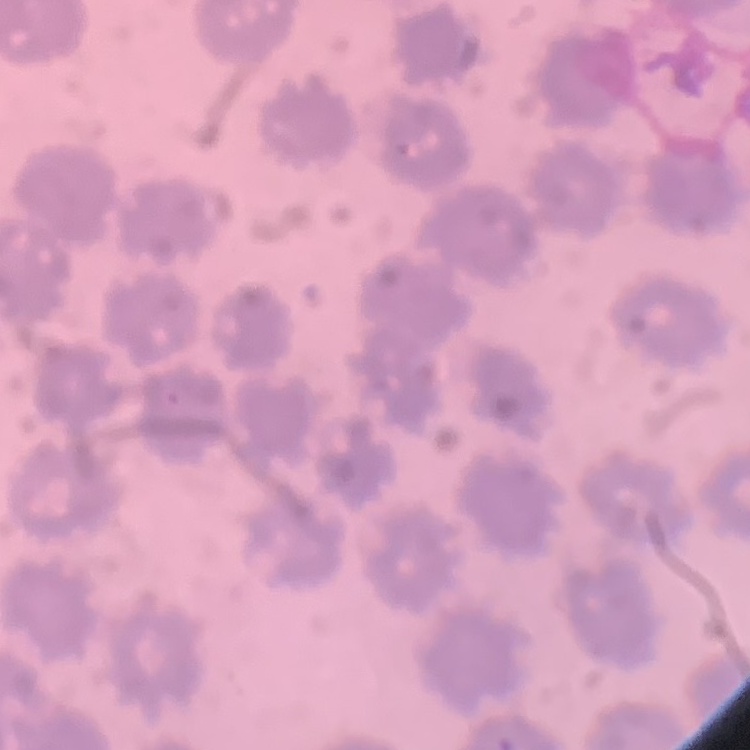

Summary:
  - Red blood cell morphology: no rouleaux formation
  - Preparation: thin blood smear
  - Stain: Field's or Giemsa
  - Image type: square crop of a larger photomicrograph